Classify this cell by malaria status.
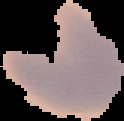

Parasitized.

Image is 124×121 pixels. From a thin blood smear. The area outside the segmented cell region is set to black.